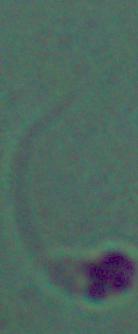
Summary:
  - Magnification: 1000x
  - Identification: Leishmania
  - Modality: photomicrograph